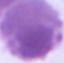
Summary:
  - Identification: erythrocyte
  - Modality: micrograph
  - Magnification: 1000x